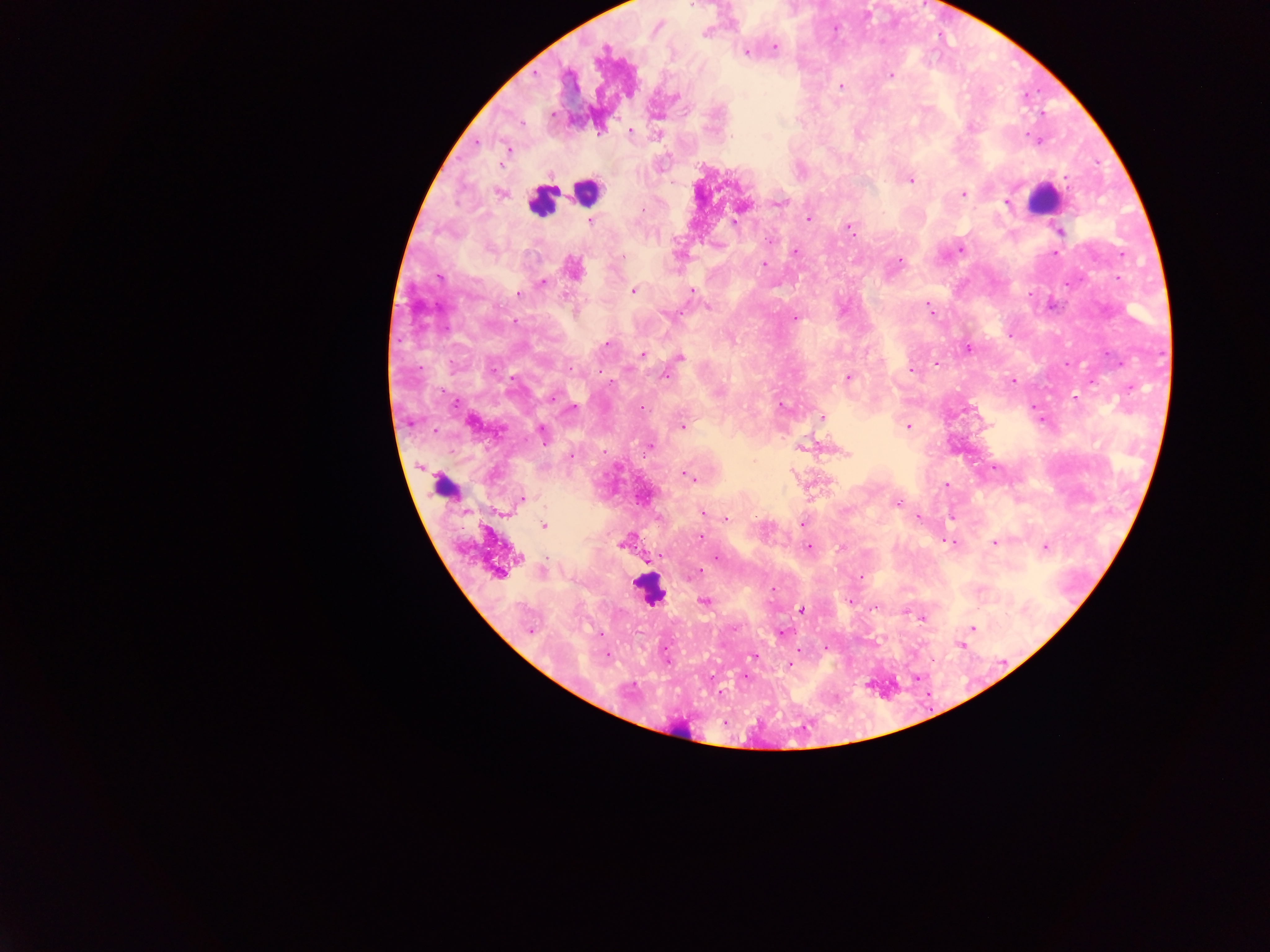
country = Ghana
image size = 1270×952 pixels
Plasmodium parasite locations = approximate centers as (x, y) in pixels: (705, 33), (774, 47), (748, 52), (891, 74), (841, 86), (926, 107), (631, 131), (600, 132), (767, 137), (508, 149), (729, 181), (911, 181), (498, 193), (963, 194), (783, 203), (1006, 203), (746, 208), (643, 209), (809, 217), (590, 221), (735, 222), (848, 229), (1060, 233), (794, 252), (1056, 253), (619, 256), (901, 259), (764, 264), (441, 277), (541, 283), (632, 290), (693, 292), (519, 293), (707, 305), (928, 306), (578, 313), (664, 315), (796, 318), (967, 346), (606, 347), (643, 353), (648, 353), (681, 357), (936, 360), (1065, 363), (912, 369), (666, 374), (848, 377), (1010, 380), (1074, 399), (454, 403), (786, 406), (642, 407), (1036, 407), (571, 408), (820, 418), (683, 425), (909, 426), (434, 432), (542, 434), (802, 447), (648, 448), (844, 452), (571, 456), (684, 472), (791, 472), (689, 476), (693, 480), (829, 482), (945, 485), (523, 498), (895, 502), (507, 514), (703, 514), (917, 517), (726, 519), (544, 527), (701, 537), (625, 542), (952, 544), (994, 544), (620, 546), (810, 546), (1045, 546), (1044, 550), (718, 558), (515, 561), (699, 571), (861, 575), (634, 583), (704, 601), (800, 610), (925, 618), (972, 629), (530, 631), (781, 633), (606, 656), (753, 657), (788, 664)
capture = mobile-phone photograph through a microscope
field of view = single
preparation = thick blood film